Classify this cell by malaria status.
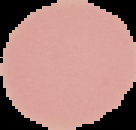
Uninfected.

image size = 136×130 pixels
preparation = thin blood film
image type = segmented cell region on a black background